Classify this cell by malaria status.
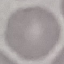

Uninfected.

Summary:
  - Image type: cell patch, automatically extracted from a larger field of view and resized to 64 × 64 pixels
  - Preparation: thin blood film
  - Capture: smartphone through the microscope eyepiece
  - Stain: Giemsa